Point out Plasmodium parasites and leukocytes.
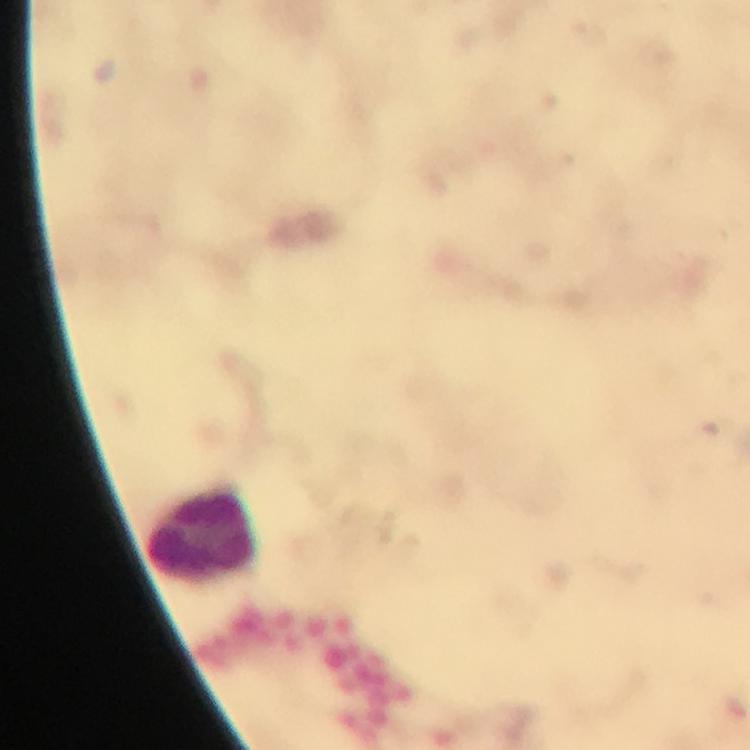
No Plasmodium parasites seen.
Approximate object centers, in pixels from the top-left corner.
Leukocytes: (x=202, y=535).

preparation = thick smear
image size = 750×750 pixels
cropped from = a single field of view
magnification = 100x
immersion oil = used
stain = Giemsa
capture = smartphone mounted on the microscope
context = from a malaria diagnostic workup